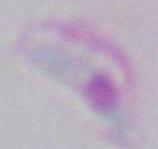
identification = Toxoplasma gondii
magnification = 1000x
modality = photomicrograph